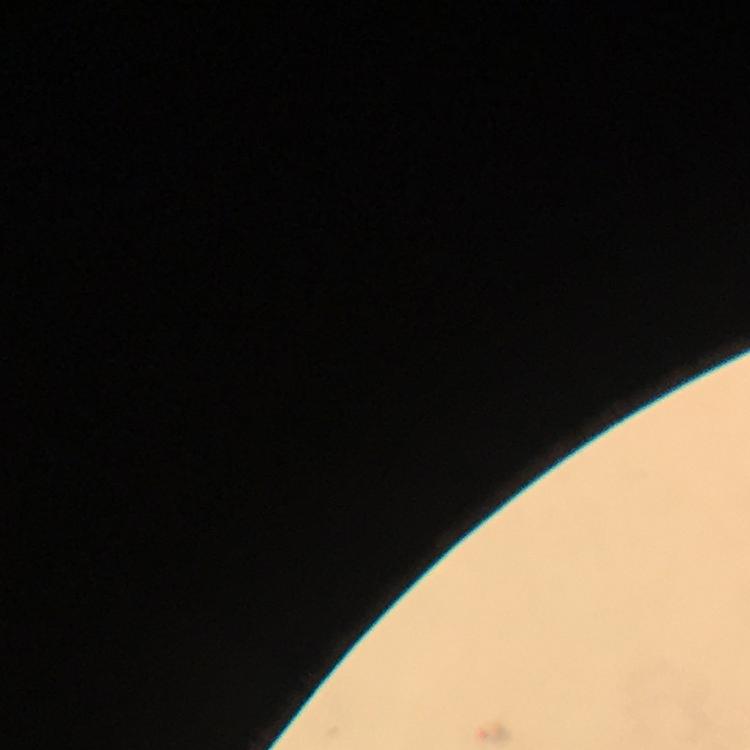
Approximate centers as [x, y] in pixels.
Summary:
  - Plasmodium parasite locations: [494, 734]
  - Image size: 750×750 pixels
  - Magnification: 100x
  - Immersion oil: used
  - Context: from a malaria diagnostic workup
  - Capture: smartphone camera through the microscope
  - Cropped from: one field of view
  - Preparation: thick blood film
  - Stain: Giemsa